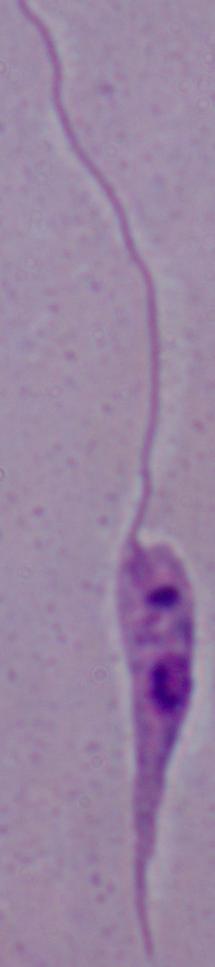

1000x magnification. A Leishmania parasite is shown. Photomicrograph.